Point out each Plasmodium parasite.
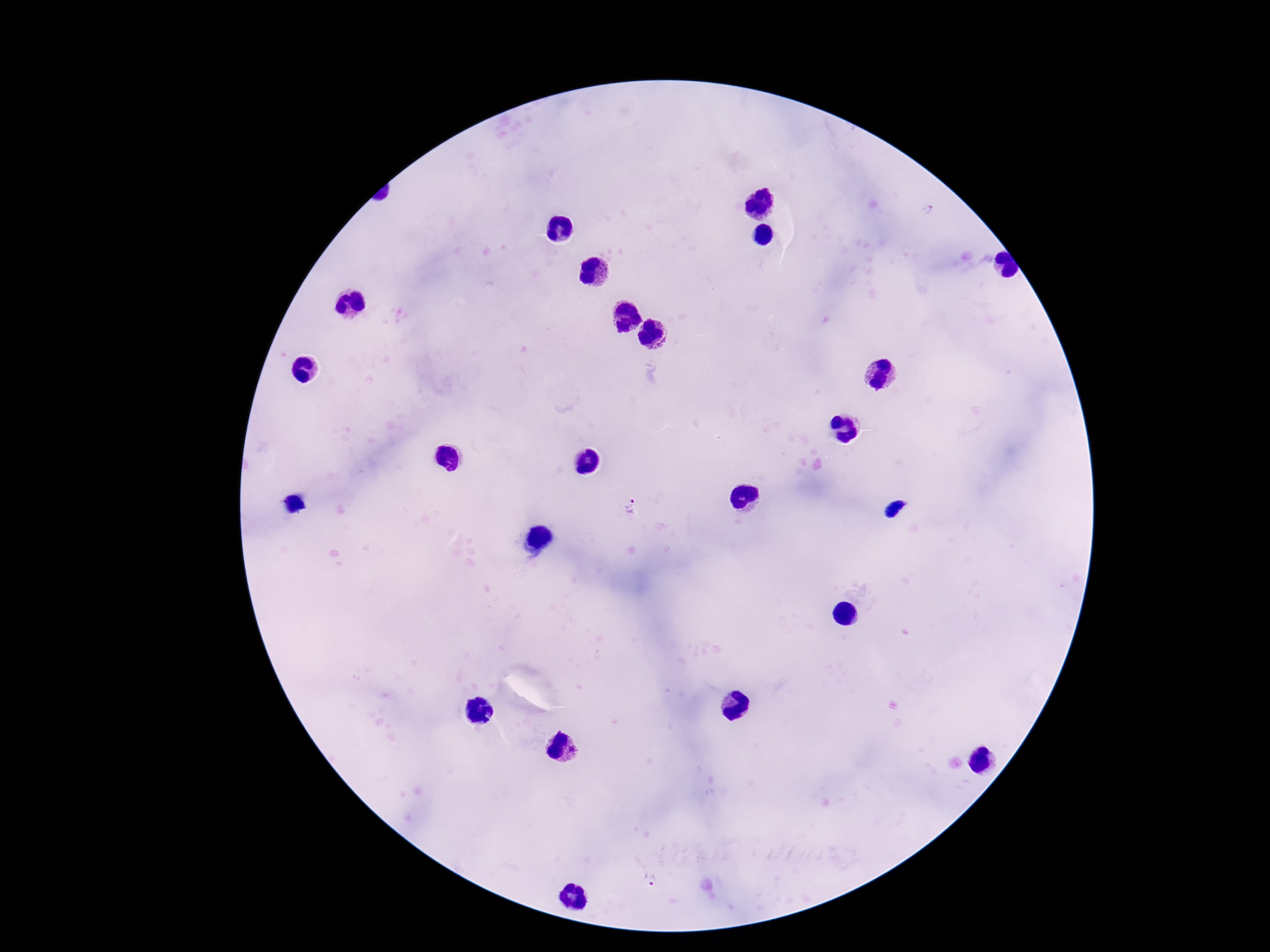
Approximate object centers, in pixels from the top-left corner.
Plasmodium parasites: (x=927, y=212), (x=632, y=505), (x=649, y=880).

magnification: 100x
image_size: 1270×952 pixels
stain: Giemsa
capture: smartphone camera through the microscope eyepiece
field_of_view: one from this slide
preparation: thick blood smear
patient_malaria_status: positive